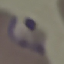 Result: malaria parasites identified. Giemsa stain. Photographed with a smartphone camera at the microscope eyepiece. Automatically extracted cell patch, resized to 64 × 64 pixels. Thin smear of blood.